State which parasite is depicted.
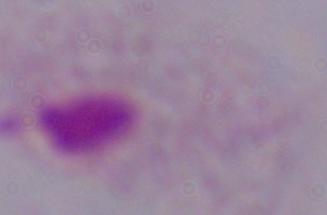

This is a trichomonad.

magnification = 1000x
modality = photomicrograph